Name the parasite shown.
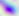

Toxoplasma gondii.

magnification = 400x
modality = micrograph